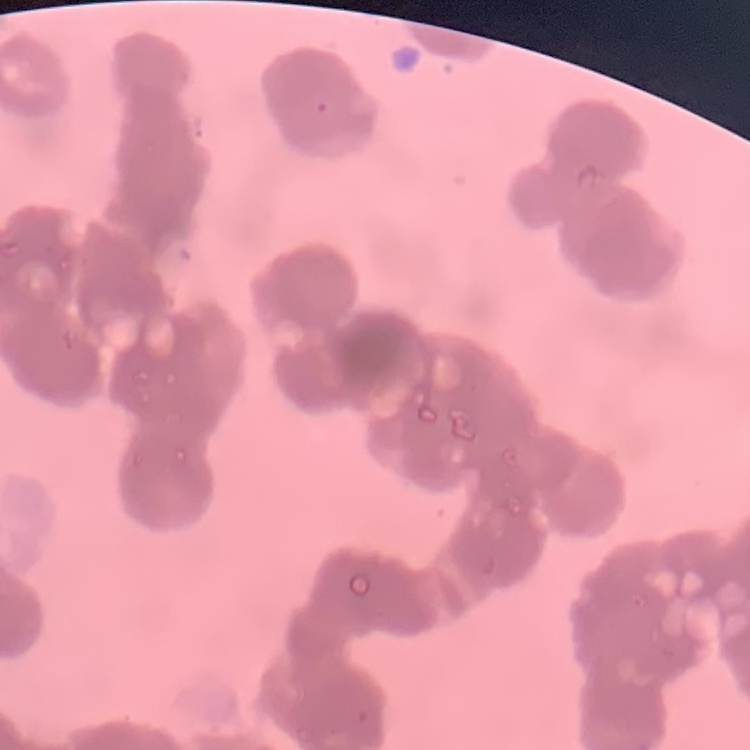
{
  "erythrocyte_morphology": "rouleaux formation",
  "stain": "Field's or Giemsa",
  "preparation": "thin blood film",
  "image_type": "one tile cut from a larger photomicrograph"
}